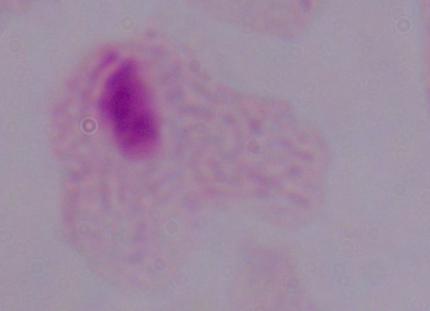
Summary:
  - Identification: trichomonad
  - Magnification: 1000x
  - Modality: micrograph